Report the malaria status of this cell.
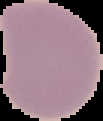
Uninfected.

Summary:
  - Image type: segmented cell region on a black background
  - Image size: 103×121 pixels
  - Preparation: thin blood film